Locate every Plasmodium falciparum-infected red blood cell.
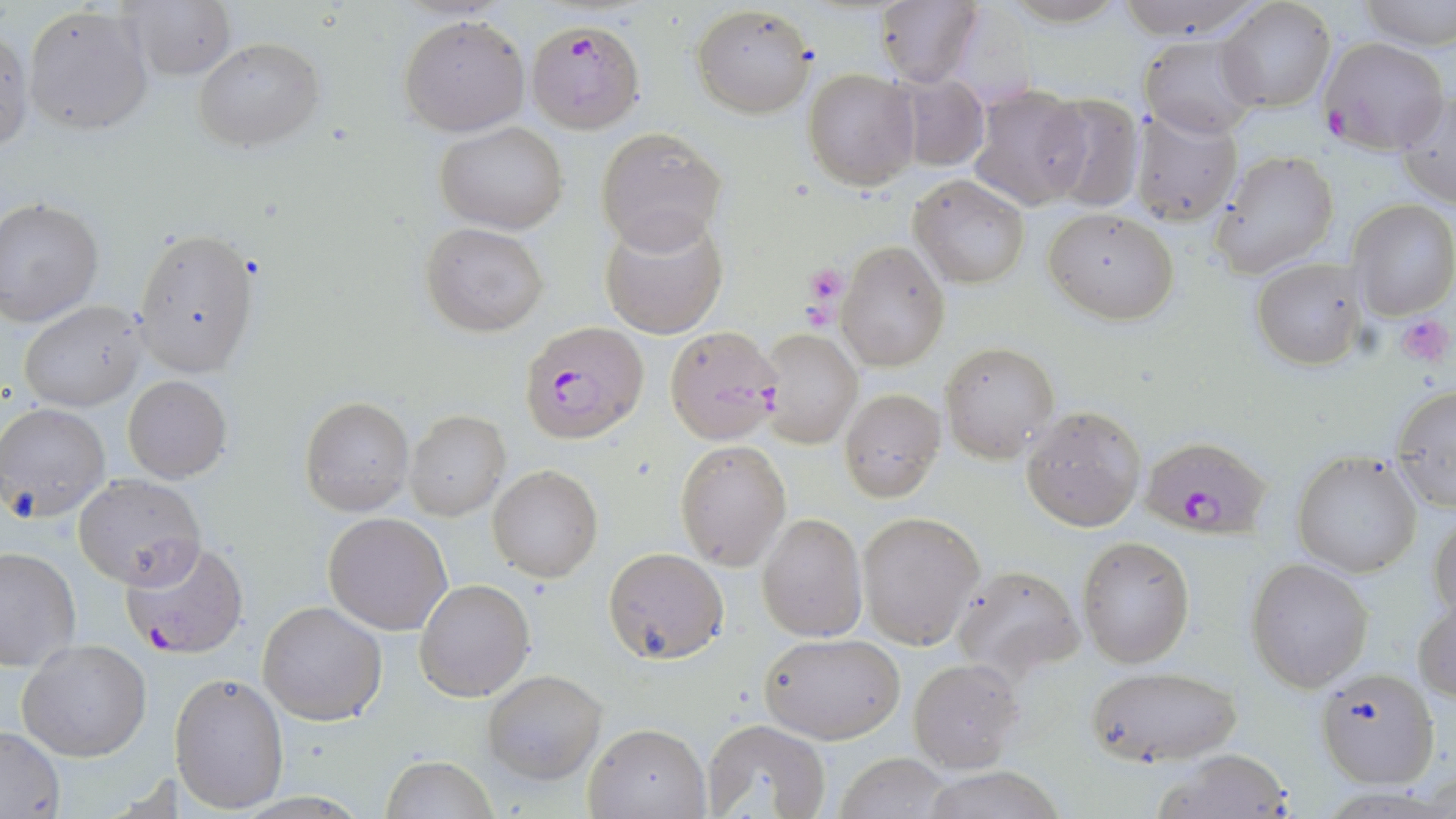

Approximate bounding boxes as [x1, y1, x2, y2] in pixels.
Plasmodium falciparum-infected red blood cells: [526, 17, 646, 135], [1319, 36, 1450, 156], [518, 321, 647, 443], [1143, 436, 1272, 539], [121, 538, 249, 660].

slide-level diagnosis = Plasmodium falciparum
magnification = 1000x
image size = 1456×819 pixels
platelet locations = approximate bounding boxes as [x1, y1, x2, y2] in pixels: [801, 260, 847, 309], [1394, 311, 1455, 366]
preparation = thin blood film
field of view = one of a larger specimen
stain = May-Grünwald-Giemsa
modality = optical microscopy
uninfected red blood cell locations = approximate bounding boxes as [x1, y1, x2, y2] in pixels: [874, 0, 982, 89], [1110, 0, 1267, 40], [1358, 0, 1456, 49], [1216, 1, 1335, 115], [117, 3, 236, 81], [22, 4, 155, 136], [690, 4, 816, 117], [398, 14, 530, 136], [0, 23, 31, 159], [1141, 34, 1262, 140], [193, 36, 325, 152], [804, 69, 919, 190], [895, 73, 991, 170], [968, 84, 1091, 210], [1395, 85, 1456, 208], [1036, 93, 1144, 211], [1132, 104, 1244, 227], [436, 121, 568, 233], [596, 127, 726, 251], [1212, 148, 1339, 277], [909, 174, 1030, 289], [0, 199, 103, 326], [1349, 200, 1456, 319], [1043, 207, 1179, 323], [599, 211, 729, 339], [421, 221, 549, 335], [133, 227, 260, 377], [836, 242, 950, 370], [1251, 257, 1366, 370], [17, 300, 145, 411], [662, 325, 783, 444], [759, 327, 862, 448], [940, 343, 1059, 463], [122, 374, 232, 483], [1390, 384, 1456, 512], [840, 388, 945, 501], [300, 395, 415, 518], [0, 402, 110, 516], [1020, 405, 1147, 532], [405, 410, 510, 520], [675, 438, 793, 572], [1292, 452, 1423, 577], [488, 464, 603, 582], [73, 474, 204, 589], [1429, 507, 1456, 625], [857, 511, 984, 650], [322, 512, 454, 636], [756, 513, 865, 642], [1077, 537, 1193, 667], [0, 545, 81, 674], [603, 546, 728, 665], [1246, 557, 1374, 692], [949, 562, 1083, 683], [414, 578, 534, 702], [1413, 595, 1456, 704], [257, 600, 387, 726], [758, 632, 905, 744], [17, 638, 152, 762], [909, 658, 1024, 774], [1082, 664, 1244, 766], [1316, 666, 1440, 787], [482, 669, 609, 784], [169, 671, 290, 813], [703, 717, 833, 819], [584, 723, 710, 818], [0, 727, 65, 816], [1157, 749, 1292, 819], [836, 752, 953, 819], [382, 755, 496, 819], [925, 770, 1064, 819]